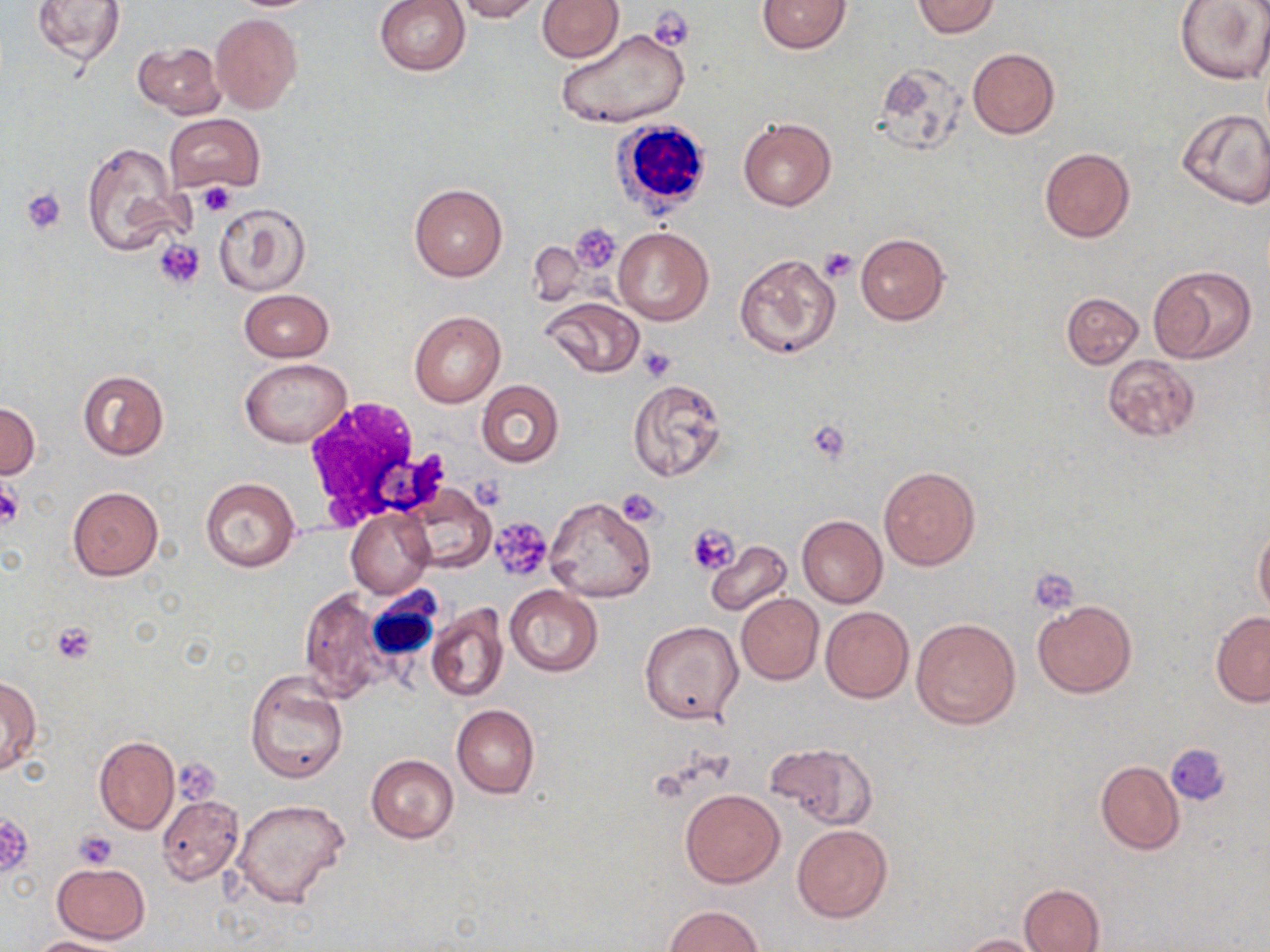

Summary:
  - Coordinate format: approximate bounding boxes as named x1/y1/x2/y2 corners in pixels
  - Platelet locations: (x1=649, y1=6, x2=694, y2=51), (x1=197, y1=183, x2=236, y2=217), (x1=19, y1=187, x2=66, y2=235), (x1=571, y1=224, x2=622, y2=273), (x1=154, y1=239, x2=205, y2=290), (x1=818, y1=247, x2=857, y2=283), (x1=638, y1=346, x2=676, y2=382), (x1=806, y1=420, x2=852, y2=464), (x1=0, y1=484, x2=22, y2=530), (x1=616, y1=488, x2=664, y2=528), (x1=488, y1=518, x2=552, y2=581), (x1=688, y1=523, x2=740, y2=576), (x1=1029, y1=569, x2=1079, y2=614), (x1=51, y1=620, x2=99, y2=665), (x1=1167, y1=744, x2=1231, y2=805), (x1=173, y1=758, x2=222, y2=803), (x1=0, y1=813, x2=35, y2=879), (x1=73, y1=829, x2=117, y2=867)
  - Uninfected red blood cell locations: (x1=31, y1=0, x2=127, y2=66), (x1=374, y1=0, x2=470, y2=76), (x1=454, y1=0, x2=542, y2=22), (x1=536, y1=0, x2=623, y2=61), (x1=757, y1=0, x2=853, y2=53), (x1=911, y1=0, x2=1001, y2=37), (x1=1175, y1=0, x2=1270, y2=85), (x1=211, y1=13, x2=303, y2=115), (x1=557, y1=26, x2=691, y2=130), (x1=133, y1=40, x2=224, y2=118), (x1=967, y1=48, x2=1060, y2=138), (x1=871, y1=61, x2=966, y2=154), (x1=1176, y1=109, x2=1270, y2=207), (x1=165, y1=114, x2=265, y2=195), (x1=738, y1=115, x2=837, y2=211), (x1=81, y1=140, x2=189, y2=256), (x1=1040, y1=147, x2=1135, y2=243), (x1=409, y1=183, x2=507, y2=282), (x1=214, y1=201, x2=312, y2=296), (x1=612, y1=227, x2=714, y2=326), (x1=855, y1=233, x2=950, y2=325), (x1=527, y1=239, x2=586, y2=308), (x1=732, y1=252, x2=840, y2=360), (x1=1148, y1=265, x2=1256, y2=363), (x1=239, y1=289, x2=333, y2=362), (x1=1060, y1=292, x2=1144, y2=369), (x1=542, y1=296, x2=644, y2=377), (x1=409, y1=311, x2=505, y2=407), (x1=1102, y1=355, x2=1201, y2=442), (x1=240, y1=358, x2=350, y2=448), (x1=77, y1=371, x2=169, y2=460), (x1=628, y1=378, x2=727, y2=483), (x1=476, y1=379, x2=565, y2=467), (x1=0, y1=401, x2=40, y2=478), (x1=878, y1=465, x2=981, y2=569), (x1=199, y1=477, x2=301, y2=572), (x1=67, y1=486, x2=163, y2=581), (x1=407, y1=487, x2=497, y2=573), (x1=542, y1=496, x2=656, y2=604), (x1=347, y1=508, x2=433, y2=598), (x1=796, y1=515, x2=888, y2=607), (x1=1254, y1=523, x2=1270, y2=621), (x1=706, y1=541, x2=792, y2=617), (x1=504, y1=585, x2=602, y2=676), (x1=297, y1=588, x2=392, y2=699), (x1=736, y1=593, x2=823, y2=684), (x1=1032, y1=601, x2=1137, y2=697), (x1=425, y1=603, x2=509, y2=702), (x1=820, y1=607, x2=913, y2=702), (x1=1211, y1=612, x2=1270, y2=705), (x1=911, y1=617, x2=1021, y2=730), (x1=641, y1=620, x2=745, y2=725), (x1=245, y1=669, x2=348, y2=784), (x1=0, y1=675, x2=41, y2=774), (x1=452, y1=705, x2=540, y2=798), (x1=94, y1=736, x2=179, y2=834), (x1=765, y1=742, x2=877, y2=829), (x1=366, y1=754, x2=458, y2=843), (x1=1096, y1=760, x2=1184, y2=854), (x1=680, y1=788, x2=784, y2=887), (x1=157, y1=795, x2=243, y2=885), (x1=230, y1=799, x2=350, y2=908), (x1=792, y1=824, x2=892, y2=923), (x1=53, y1=861, x2=150, y2=944), (x1=1019, y1=883, x2=1104, y2=952), (x1=663, y1=904, x2=763, y2=952), (x1=959, y1=934, x2=1050, y2=952), (x1=28, y1=936, x2=126, y2=952)
  - White blood cell locations: (x1=609, y1=118, x2=715, y2=216), (x1=303, y1=398, x2=443, y2=531), (x1=370, y1=582, x2=445, y2=660)
  - Slide-level diagnosis: negative for blood parasites
  - Modality: optical microscopy
  - Field of view: single
  - Image size: 1270×952 pixels
  - Stain: May-Grünwald-Giemsa
  - Preparation: thin blood smear
  - Magnification: 1000x